Describe the morphology of the erythrocytes.
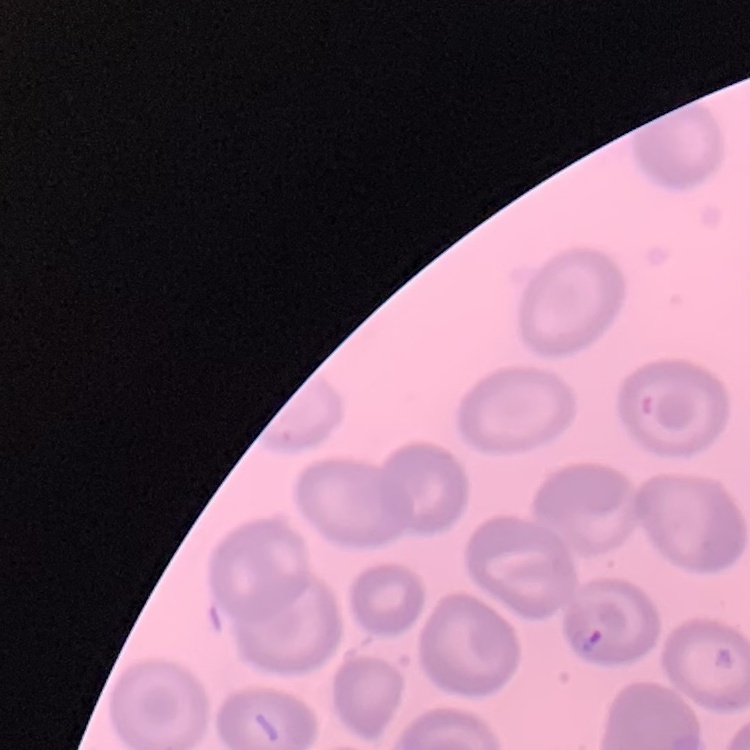

No rouleaux formation.

Thin blood smear. Stained with either Field's or Giemsa. One tile cut from a larger photomicrograph.